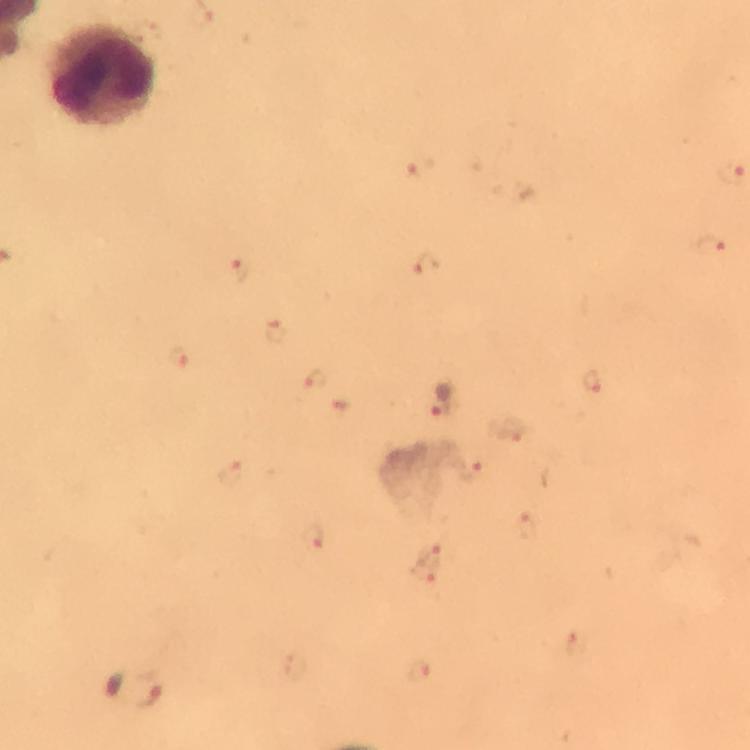 Approximate object centers, in pixels from the top-left corner. Leukocyte locations: (x=106, y=76). Plasmodium parasite locations: (x=714, y=249), (x=426, y=263), (x=241, y=269), (x=277, y=329), (x=175, y=357), (x=313, y=379), (x=591, y=380), (x=445, y=402), (x=233, y=472), (x=313, y=536), (x=133, y=688). A crop from one field of view. Giemsa-stained preparation. At 100x magnification. Image is 750×750 pixels. Thick blood film. Smartphone photograph taken through a microscope. Immersion oil was used. From a diagnostic examination for malaria.